Report the malaria status of this cell.
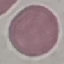
It is uninfected.

{
  "preparation": "thin smear",
  "image_type": "automatically extracted cell patch, resized to 64 × 64 pixels",
  "stain": "Giemsa",
  "capture": "smartphone camera at the microscope eyepiece"
}